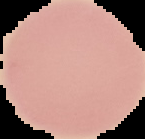
Result: negative for Plasmodium parasites. Image is 145×139 pixels. From a thin blood film. Cell region segmented out of the field of view; the surrounding area is masked to black.